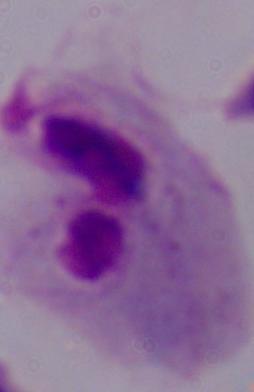
1000x magnification. Photomicrograph. A trichomonad is shown.